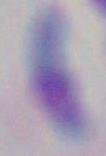
Photomicrograph. 1000x magnification. Toxoplasma gondii is shown.